Describe the morphology of the erythrocytes.
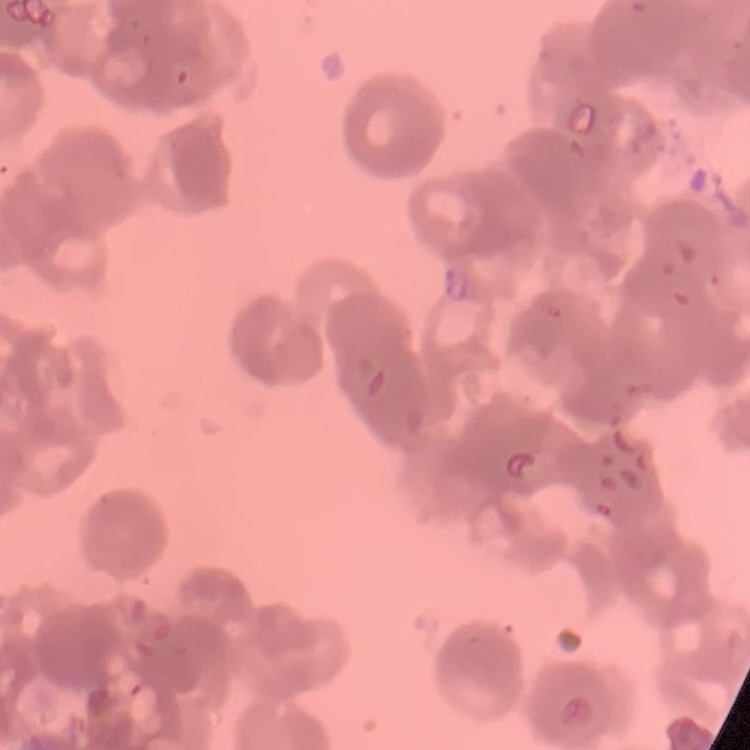
They show rouleaux formation.

Summary:
  - Preparation: thin blood smear
  - Stain: Field's or Giemsa
  - Image type: square crop of a larger photomicrograph